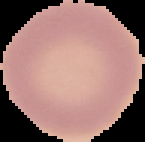
image type = cell region segmented out of the field of view; surrounding area masked to black
preparation = thin blood film
image size = 145×142 pixels
malaria status = uninfected